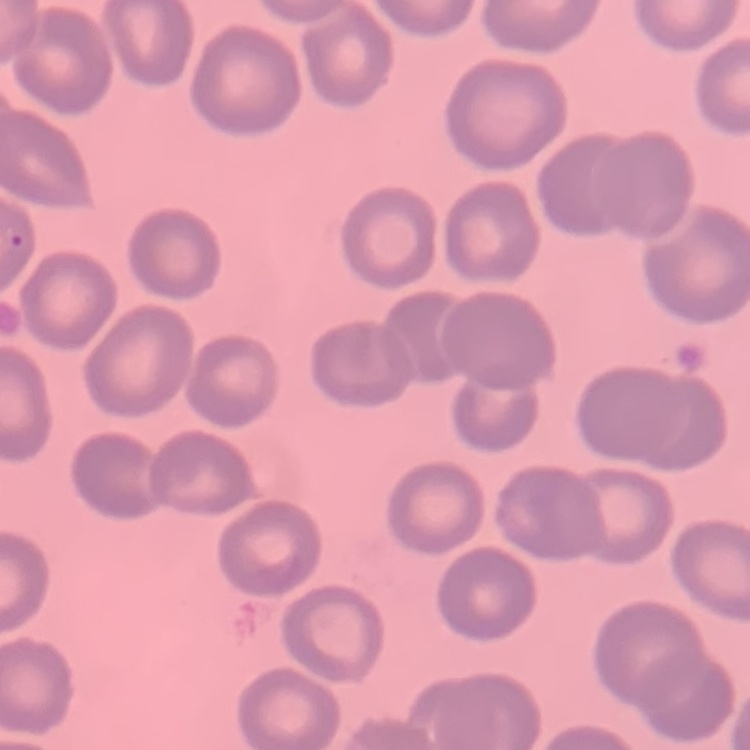

erythrocyte morphology = no rouleaux formation
stain = Field's or Giemsa
image type = one tile cut from a larger photomicrograph
preparation = thin blood smear